Evaluate for malaria.
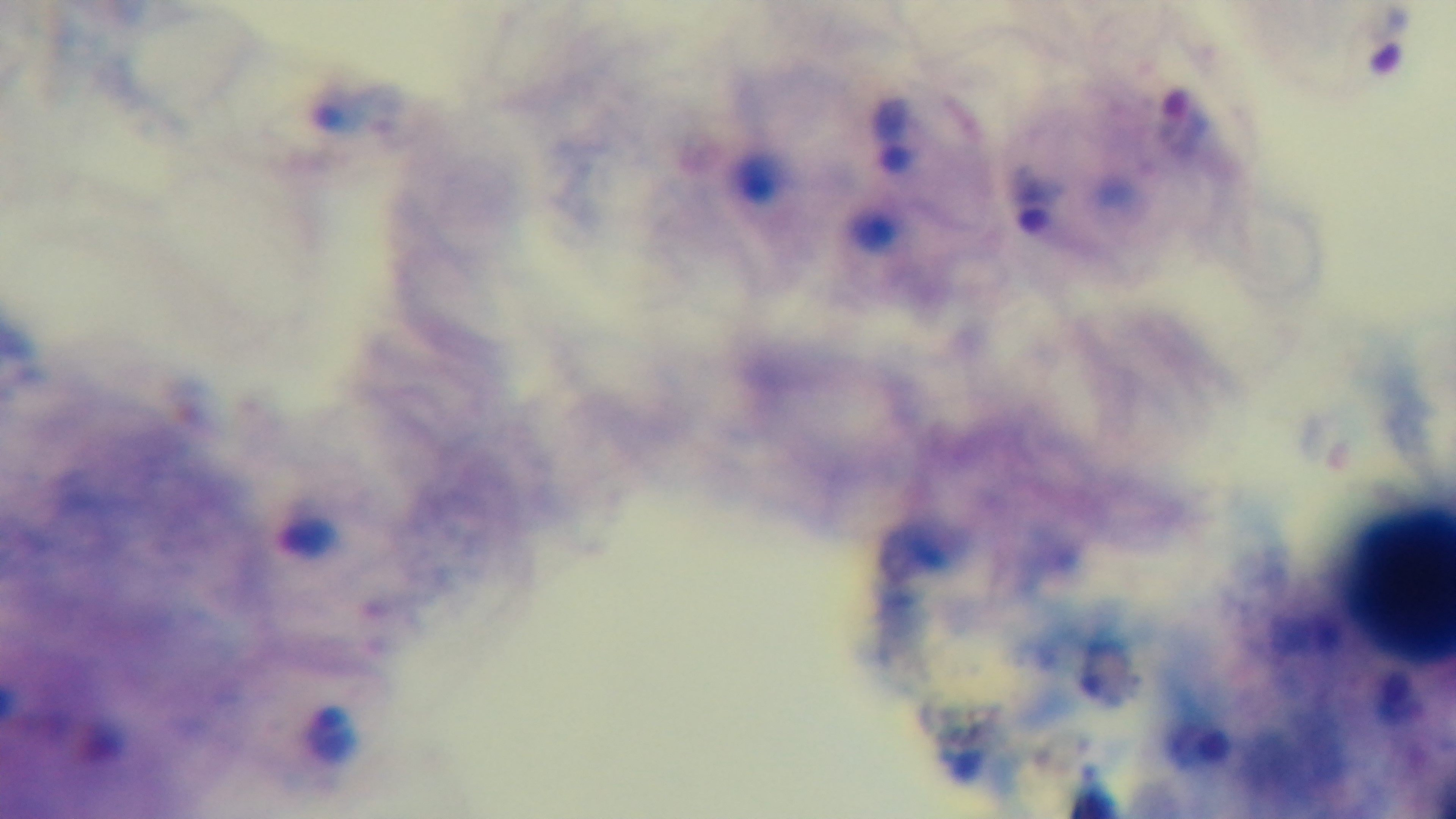

It is infected.

preparation = thick
stain = Giemsa
objective = 100x oil immersion
field of view = single
modality = light microscopy
capture = mounted 4K digital camera